Locate every malaria parasite.
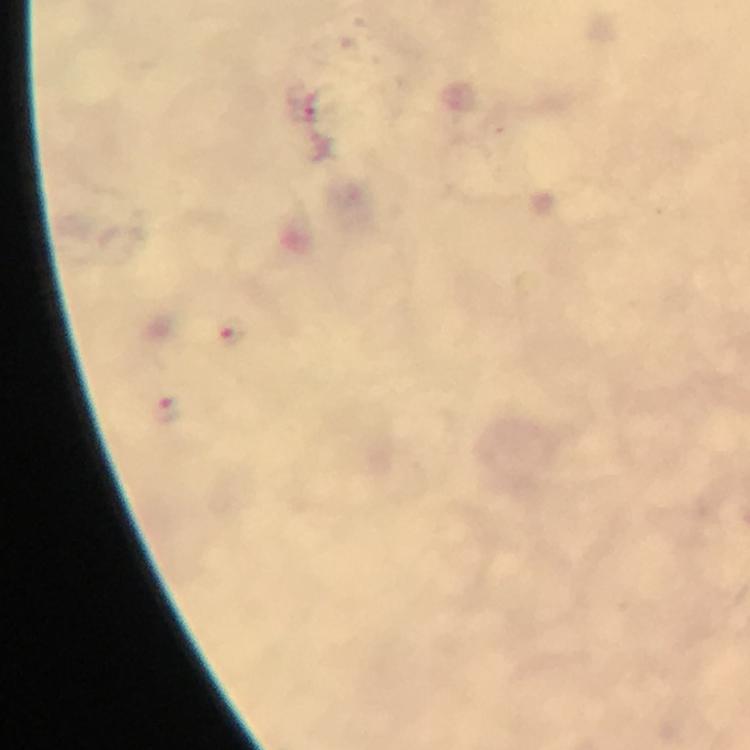
Approximate object centers, in pixels from the top-left corner.
Malaria parasites: (x=308, y=109), (x=233, y=333), (x=166, y=406).

Summary:
  - Immersion oil: used
  - Stain: Giemsa
  - Cropped from: a single field of view
  - Magnification: 100x
  - Image size: 750×750 pixels
  - Context: from a malaria diagnostic workup
  - Preparation: thick smear
  - Capture: smartphone photograph through a microscope